Assess the morphology of the erythrocytes.
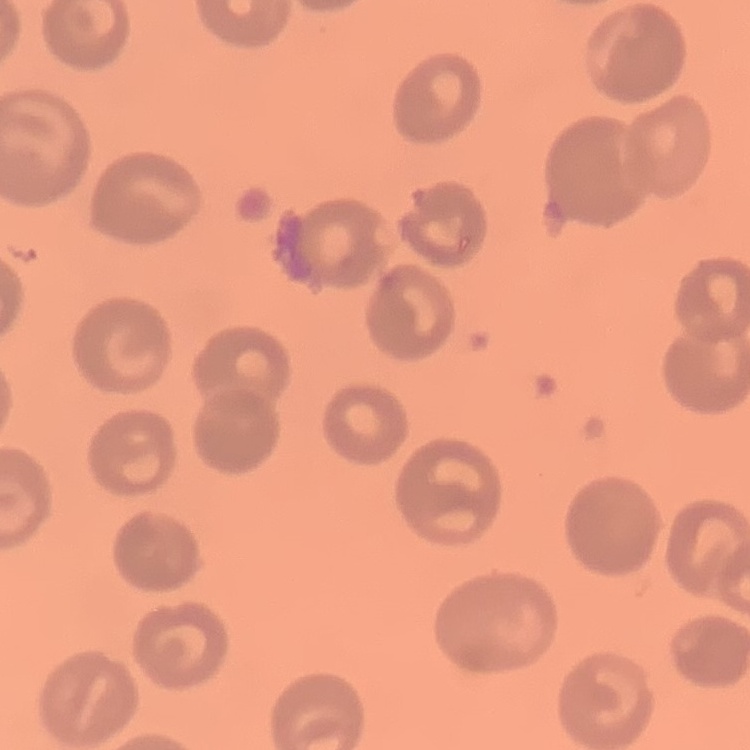

No rouleaux formation.

Stained with either Field's or Giemsa. Square crop of a larger photomicrograph. Thin blood smear.